Locate and identify every blood parasite.
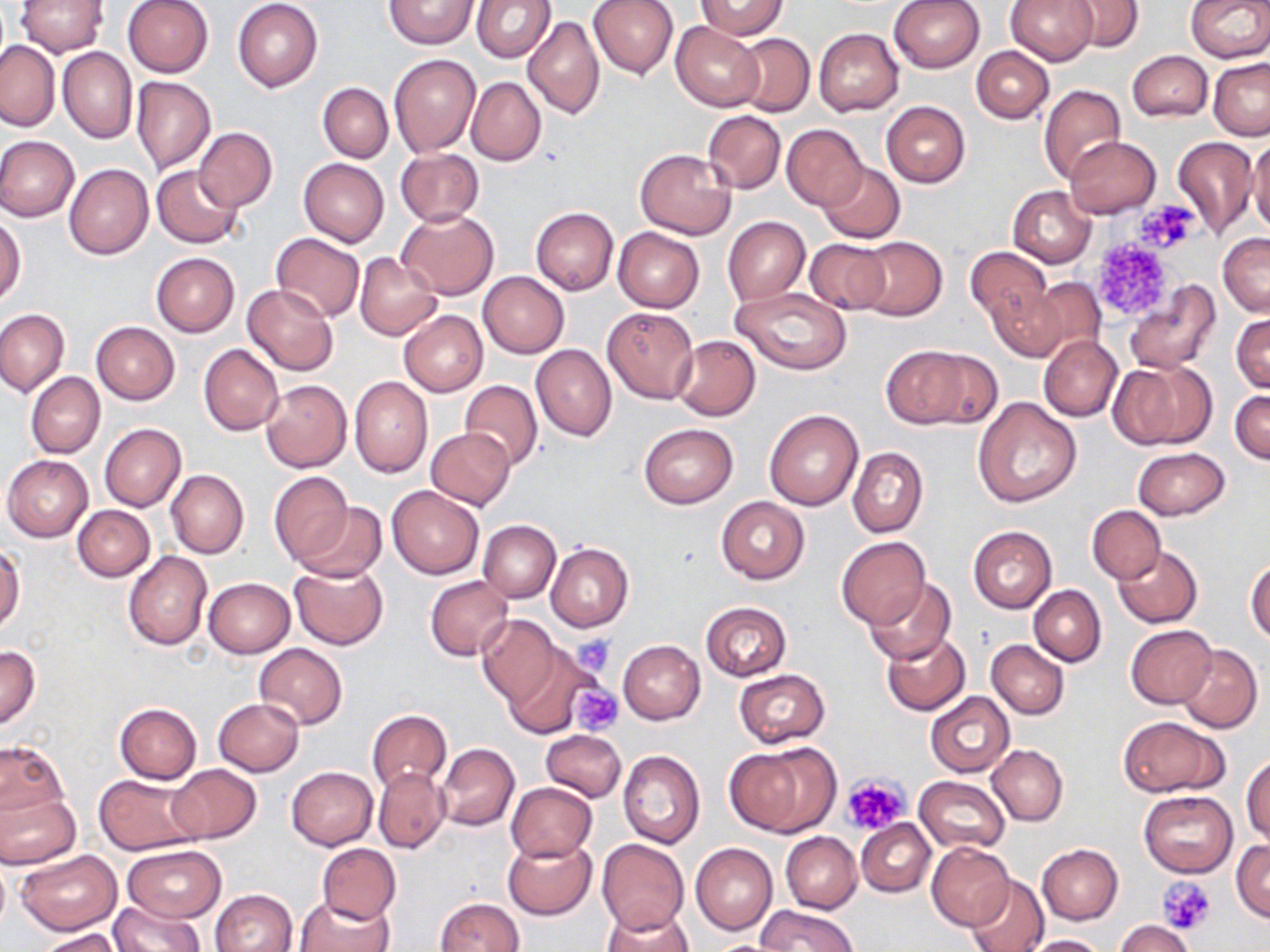

No blood parasites observed.

slide_level_diagnosis: negative for blood parasites
stain: May-Grünwald-Giemsa
modality: light microscopy
uninfected_red_blood_cell_locations: 'approximate bounding boxes as named x1/y1/x2/y2 corners in pixels: (x1=122, y1=0, x2=214, y2=78), (x1=233, y1=0, x2=323, y2=91), (x1=471, y1=0, x2=555, y2=63), (x1=587, y1=0, x2=678, y2=78), (x1=888, y1=0, x2=987, y2=73), (x1=1006, y1=0, x2=1097, y2=66), (x1=1185, y1=0, x2=1269, y2=63), (x1=14, y1=1, x2=107, y2=56), (x1=385, y1=1, x2=477, y2=49), (x1=1067, y1=1, x2=1144, y2=53), (x1=697, y1=2, x2=788, y2=39), (x1=523, y1=17, x2=605, y2=120), (x1=671, y1=20, x2=764, y2=111), (x1=814, y1=28, x2=905, y2=117), (x1=732, y1=33, x2=814, y2=117), (x1=0, y1=40, x2=59, y2=130), (x1=972, y1=47, x2=1053, y2=124), (x1=58, y1=48, x2=136, y2=142), (x1=1126, y1=51, x2=1212, y2=122), (x1=389, y1=53, x2=482, y2=156), (x1=1208, y1=59, x2=1270, y2=140), (x1=130, y1=77, x2=216, y2=174), (x1=466, y1=77, x2=546, y2=166), (x1=318, y1=82, x2=393, y2=162), (x1=1038, y1=83, x2=1127, y2=184), (x1=882, y1=101, x2=970, y2=187), (x1=702, y1=110, x2=785, y2=194), (x1=781, y1=123, x2=869, y2=211), (x1=193, y1=128, x2=277, y2=213), (x1=1170, y1=135, x2=1258, y2=238), (x1=0, y1=136, x2=79, y2=221), (x1=1247, y1=136, x2=1270, y2=235), (x1=1065, y1=137, x2=1160, y2=218), (x1=634, y1=148, x2=737, y2=238), (x1=395, y1=149, x2=484, y2=227), (x1=299, y1=158, x2=389, y2=246), (x1=817, y1=162, x2=904, y2=242), (x1=64, y1=164, x2=153, y2=259), (x1=153, y1=164, x2=243, y2=248), (x1=1007, y1=185, x2=1096, y2=268), (x1=531, y1=207, x2=619, y2=294), (x1=397, y1=210, x2=499, y2=300), (x1=0, y1=215, x2=23, y2=307), (x1=723, y1=215, x2=810, y2=304), (x1=614, y1=227, x2=705, y2=312), (x1=270, y1=233, x2=365, y2=322), (x1=1218, y1=233, x2=1270, y2=316), (x1=850, y1=236, x2=947, y2=321), (x1=803, y1=238, x2=892, y2=314), (x1=964, y1=247, x2=1054, y2=326), (x1=354, y1=252, x2=444, y2=341), (x1=151, y1=253, x2=239, y2=336), (x1=478, y1=272, x2=569, y2=358), (x1=1023, y1=275, x2=1107, y2=359), (x1=1124, y1=280, x2=1221, y2=374), (x1=243, y1=284, x2=337, y2=375), (x1=730, y1=285, x2=853, y2=375), (x1=986, y1=285, x2=1067, y2=362), (x1=602, y1=305, x2=700, y2=402), (x1=0, y1=308, x2=69, y2=397), (x1=399, y1=310, x2=488, y2=397), (x1=1232, y1=313, x2=1269, y2=393), (x1=91, y1=321, x2=179, y2=404), (x1=671, y1=335, x2=761, y2=421), (x1=1038, y1=335, x2=1122, y2=421), (x1=199, y1=344, x2=283, y2=436), (x1=531, y1=345, x2=617, y2=441), (x1=882, y1=345, x2=986, y2=429), (x1=1109, y1=359, x2=1215, y2=449), (x1=26, y1=372, x2=105, y2=459), (x1=350, y1=376, x2=432, y2=477), (x1=261, y1=379, x2=352, y2=473), (x1=460, y1=380, x2=543, y2=470), (x1=1231, y1=389, x2=1270, y2=463), (x1=974, y1=397, x2=1080, y2=506), (x1=764, y1=408, x2=864, y2=511), (x1=637, y1=422, x2=738, y2=509), (x1=99, y1=423, x2=187, y2=511), (x1=426, y1=428, x2=516, y2=510), (x1=1132, y1=446, x2=1230, y2=520), (x1=848, y1=447, x2=928, y2=538), (x1=2, y1=455, x2=94, y2=541), (x1=167, y1=469, x2=249, y2=558), (x1=268, y1=471, x2=354, y2=565), (x1=386, y1=485, x2=485, y2=578), (x1=716, y1=496, x2=809, y2=584), (x1=296, y1=503, x2=387, y2=583), (x1=73, y1=504, x2=155, y2=581), (x1=1087, y1=505, x2=1165, y2=583), (x1=478, y1=520, x2=560, y2=603), (x1=967, y1=525, x2=1057, y2=612), (x1=837, y1=537, x2=931, y2=628), (x1=546, y1=543, x2=633, y2=631), (x1=1113, y1=544, x2=1203, y2=628), (x1=0, y1=545, x2=23, y2=635), (x1=123, y1=551, x2=212, y2=650), (x1=1247, y1=557, x2=1270, y2=643), (x1=288, y1=562, x2=389, y2=650), (x1=425, y1=575, x2=514, y2=660), (x1=203, y1=577, x2=295, y2=657), (x1=865, y1=579, x2=955, y2=664), (x1=1029, y1=586, x2=1105, y2=665), (x1=700, y1=601, x2=792, y2=681), (x1=476, y1=614, x2=560, y2=705), (x1=1125, y1=625, x2=1217, y2=708), (x1=880, y1=632, x2=970, y2=716), (x1=618, y1=639, x2=705, y2=724), (x1=986, y1=639, x2=1070, y2=719), (x1=253, y1=643, x2=347, y2=729), (x1=500, y1=644, x2=595, y2=736), (x1=1177, y1=644, x2=1262, y2=733), (x1=1, y1=646, x2=41, y2=729), (x1=735, y1=670, x2=830, y2=748), (x1=926, y1=691, x2=1015, y2=777), (x1=213, y1=698, x2=304, y2=776), (x1=115, y1=702, x2=202, y2=784), (x1=366, y1=709, x2=452, y2=793), (x1=1117, y1=716, x2=1228, y2=797), (x1=540, y1=730, x2=626, y2=802), (x1=0, y1=739, x2=68, y2=823), (x1=726, y1=742, x2=839, y2=835), (x1=435, y1=743, x2=519, y2=831), (x1=987, y1=744, x2=1067, y2=826), (x1=618, y1=749, x2=705, y2=849), (x1=1242, y1=753, x2=1270, y2=845), (x1=167, y1=763, x2=261, y2=843), (x1=286, y1=766, x2=378, y2=850), (x1=374, y1=767, x2=449, y2=852), (x1=93, y1=772, x2=203, y2=854), (x1=915, y1=776, x2=1009, y2=853), (x1=505, y1=782, x2=596, y2=862), (x1=0, y1=789, x2=81, y2=868), (x1=1138, y1=790, x2=1238, y2=877), (x1=856, y1=819, x2=935, y2=896), (x1=781, y1=832, x2=862, y2=913), (x1=502, y1=835, x2=596, y2=920), (x1=597, y1=838, x2=688, y2=934), (x1=1231, y1=840, x2=1270, y2=921), (x1=928, y1=842, x2=1015, y2=930), (x1=691, y1=843, x2=777, y2=935), (x1=122, y1=844, x2=225, y2=923), (x1=316, y1=844, x2=401, y2=923), (x1=1037, y1=844, x2=1123, y2=925), (x1=14, y1=849, x2=122, y2=935), (x1=0, y1=858, x2=10, y2=938), (x1=967, y1=876, x2=1047, y2=952), (x1=211, y1=889, x2=298, y2=952), (x1=295, y1=894, x2=393, y2=952), (x1=436, y1=898, x2=523, y2=951), (x1=109, y1=900, x2=205, y2=952), (x1=757, y1=904, x2=856, y2=951), (x1=601, y1=906, x2=694, y2=952), (x1=1115, y1=919, x2=1196, y2=952), (x1=35, y1=929, x2=122, y2=951), (x1=1027, y1=934, x2=1110, y2=952), (x1=703, y1=939, x2=791, y2=952)'
platelet_locations: 'approximate bounding boxes as named x1/y1/x2/y2 corners in pixels: (x1=1139, y1=202, x2=1198, y2=248), (x1=1088, y1=225, x2=1186, y2=323), (x1=572, y1=636, x2=616, y2=673), (x1=569, y1=683, x2=624, y2=735), (x1=842, y1=773, x2=912, y2=836), (x1=1158, y1=878, x2=1216, y2=934)'
image_size: 1270×952 pixels
preparation: thin blood smear
magnification: 1000x
field_of_view: one of a larger specimen